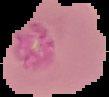

Summary:
  - Preparation: thin blood smear
  - Malaria status: uninfected
  - Image type: segmented cell region on a black background
  - Image size: 109×97 pixels